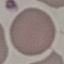

{
  "result": "no malaria parasites detected",
  "preparation": "thin smear",
  "image_type": "automatically extracted cell patch, resized to 64 × 64 pixels",
  "stain": "Giemsa",
  "capture": "smartphone camera at the microscope eyepiece"
}